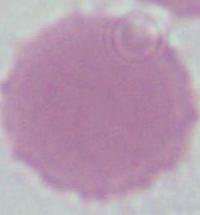
1000x magnification. Micrograph. A red blood cell is shown.